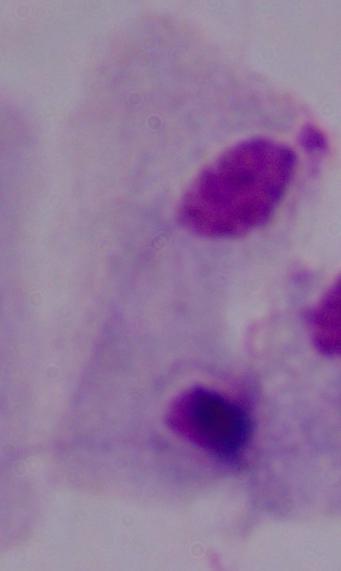
Photomicrograph. A trichomonad is seen. 1000x magnification.